Give the position of every malaria parasite.
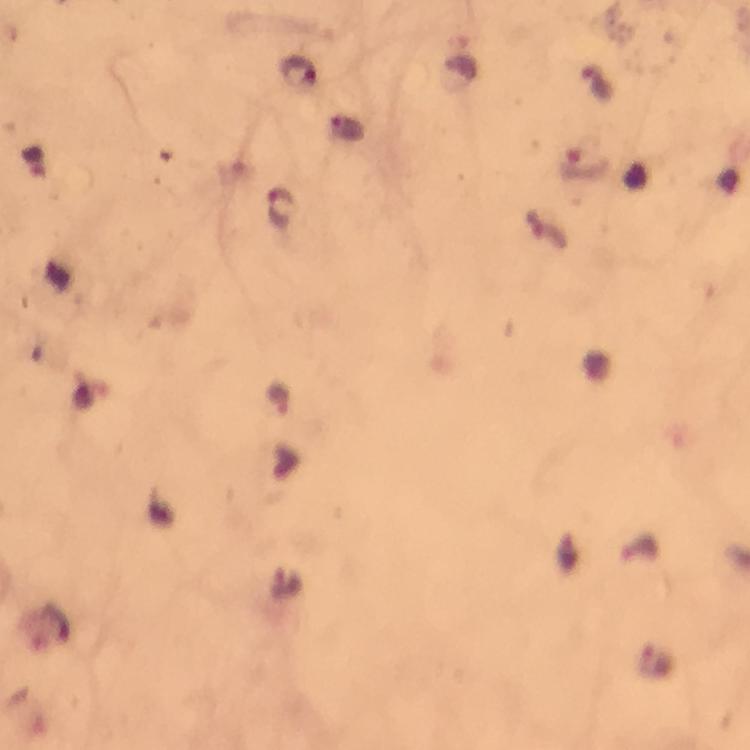

Approximate centers as [x, y] in pixels.
Malaria parasites: [299, 73], [599, 83], [585, 165], [281, 207], [640, 546], [286, 585], [655, 662].

From a malaria diagnostic workup. Cropped region of a single field of view. At 100x magnification. Thick smear. Immersion oil applied. Giemsa-stained preparation. Image is 750×750 pixels. Photographed with a smartphone mounted on the microscope.